Name the cell type shown.
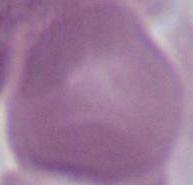

An erythrocyte.

magnification: 1000x
modality: micrograph